Give the position of every malaria parasite.
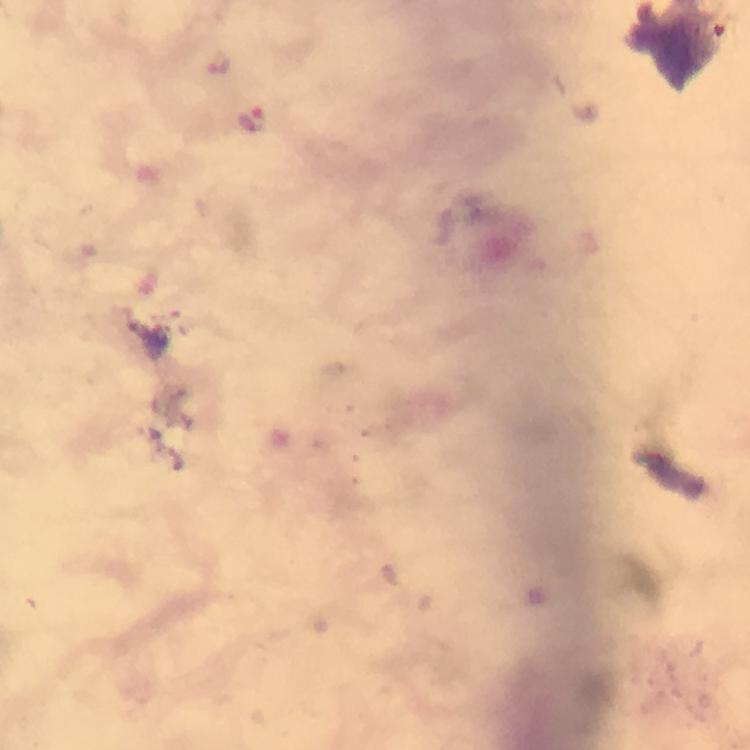
Approximate object centers, in pixels from the top-left corner.
Malaria parasites: (x=251, y=119).

Summary:
  - Immersion oil: used
  - Image size: 750×750 pixels
  - Stain: Giemsa
  - Capture: smartphone photograph through a microscope
  - Cropped from: one field of view
  - Magnification: 100x
  - Context: from a malaria diagnostic workup
  - Preparation: thick blood film